Give the extent of all Plasmodium vivax-infected red blood cells.
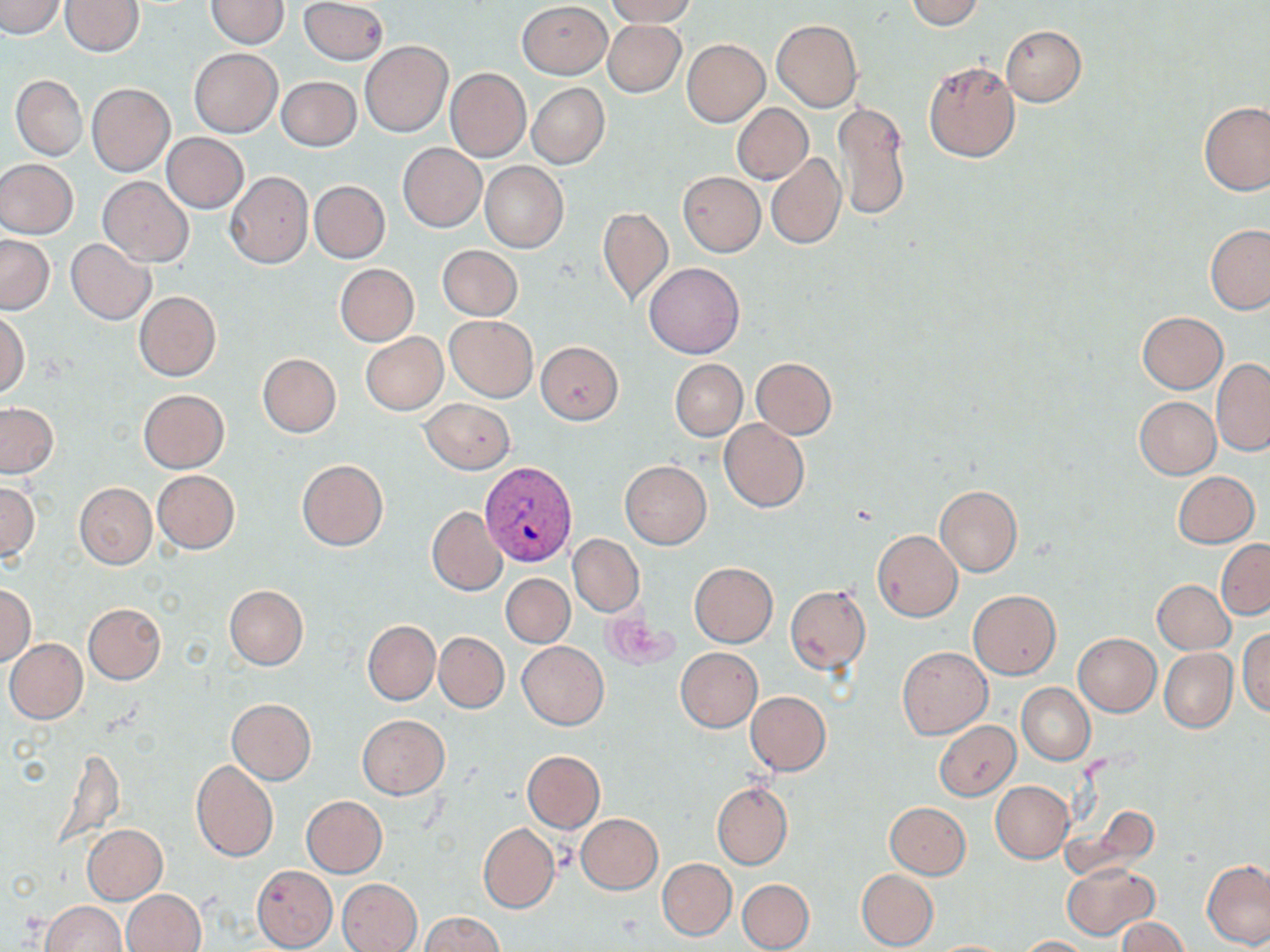
Approximate bounding boxes as named x1/y1/x2/y2 corners in pixels.
Plasmodium vivax-infected red blood cells: (x1=481, y1=461, x2=577, y2=567).

slide-level diagnosis = Plasmodium vivax
stain = May-Grünwald-Giemsa
magnification = 1000x
uninfected red blood cell locations = approximate bounding boxes as named x1/y1/x2/y2 corners in pixels: (x1=0, y1=0, x2=66, y2=38), (x1=62, y1=0, x2=143, y2=56), (x1=205, y1=0, x2=288, y2=48), (x1=604, y1=0, x2=697, y2=26), (x1=904, y1=0, x2=984, y2=29), (x1=299, y1=1, x2=388, y2=65), (x1=518, y1=1, x2=612, y2=78), (x1=771, y1=19, x2=863, y2=113), (x1=602, y1=20, x2=685, y2=96), (x1=1000, y1=25, x2=1087, y2=106), (x1=682, y1=39, x2=770, y2=127), (x1=360, y1=41, x2=452, y2=137), (x1=189, y1=49, x2=281, y2=136), (x1=924, y1=60, x2=1021, y2=163), (x1=446, y1=68, x2=531, y2=161), (x1=12, y1=75, x2=87, y2=160), (x1=277, y1=76, x2=360, y2=151), (x1=86, y1=83, x2=175, y2=177), (x1=527, y1=83, x2=609, y2=169), (x1=1198, y1=101, x2=1270, y2=195), (x1=833, y1=102, x2=910, y2=220), (x1=732, y1=103, x2=813, y2=183), (x1=162, y1=133, x2=249, y2=213), (x1=397, y1=142, x2=486, y2=232), (x1=765, y1=152, x2=846, y2=250), (x1=0, y1=158, x2=78, y2=238), (x1=480, y1=161, x2=568, y2=253), (x1=225, y1=171, x2=313, y2=268), (x1=678, y1=171, x2=764, y2=256), (x1=98, y1=178, x2=193, y2=266), (x1=309, y1=180, x2=390, y2=263), (x1=598, y1=206, x2=673, y2=309), (x1=1205, y1=224, x2=1270, y2=314), (x1=0, y1=235, x2=54, y2=315), (x1=66, y1=240, x2=155, y2=324), (x1=438, y1=245, x2=522, y2=320), (x1=644, y1=263, x2=744, y2=359), (x1=335, y1=264, x2=418, y2=345), (x1=134, y1=291, x2=221, y2=381), (x1=0, y1=311, x2=28, y2=397), (x1=1137, y1=311, x2=1229, y2=393), (x1=445, y1=316, x2=538, y2=402), (x1=360, y1=332, x2=448, y2=415), (x1=536, y1=341, x2=624, y2=424), (x1=257, y1=353, x2=342, y2=437), (x1=751, y1=357, x2=836, y2=439), (x1=670, y1=359, x2=747, y2=441), (x1=1211, y1=359, x2=1270, y2=455), (x1=138, y1=389, x2=230, y2=472), (x1=1134, y1=397, x2=1221, y2=479), (x1=420, y1=398, x2=516, y2=474), (x1=1, y1=403, x2=58, y2=477), (x1=719, y1=419, x2=810, y2=512), (x1=296, y1=459, x2=388, y2=551), (x1=620, y1=460, x2=712, y2=548), (x1=152, y1=470, x2=240, y2=554), (x1=1172, y1=471, x2=1259, y2=547), (x1=0, y1=478, x2=38, y2=564), (x1=74, y1=483, x2=156, y2=569), (x1=934, y1=485, x2=1022, y2=576), (x1=426, y1=506, x2=508, y2=596), (x1=872, y1=530, x2=963, y2=621), (x1=568, y1=534, x2=643, y2=617), (x1=1217, y1=538, x2=1270, y2=619), (x1=689, y1=562, x2=778, y2=647), (x1=501, y1=573, x2=574, y2=647), (x1=1153, y1=579, x2=1234, y2=654), (x1=1, y1=583, x2=35, y2=666), (x1=224, y1=585, x2=307, y2=670), (x1=785, y1=585, x2=870, y2=675), (x1=967, y1=590, x2=1061, y2=678), (x1=83, y1=603, x2=165, y2=685), (x1=362, y1=621, x2=440, y2=705), (x1=1237, y1=628, x2=1270, y2=717), (x1=435, y1=632, x2=509, y2=713), (x1=1073, y1=632, x2=1161, y2=716), (x1=4, y1=638, x2=88, y2=724), (x1=518, y1=642, x2=609, y2=730), (x1=897, y1=646, x2=992, y2=738), (x1=676, y1=647, x2=762, y2=732), (x1=1160, y1=647, x2=1237, y2=732), (x1=1017, y1=684, x2=1094, y2=764), (x1=745, y1=691, x2=831, y2=775), (x1=226, y1=698, x2=316, y2=784), (x1=358, y1=715, x2=449, y2=799), (x1=933, y1=721, x2=1021, y2=801), (x1=522, y1=750, x2=604, y2=833), (x1=191, y1=761, x2=279, y2=863), (x1=711, y1=781, x2=792, y2=870), (x1=991, y1=781, x2=1075, y2=863), (x1=301, y1=796, x2=387, y2=877), (x1=884, y1=802, x2=970, y2=879), (x1=1066, y1=804, x2=1155, y2=877), (x1=576, y1=814, x2=663, y2=894), (x1=478, y1=822, x2=559, y2=913), (x1=81, y1=824, x2=168, y2=904), (x1=1202, y1=858, x2=1270, y2=952), (x1=656, y1=859, x2=736, y2=940), (x1=1061, y1=862, x2=1158, y2=941), (x1=251, y1=865, x2=338, y2=951), (x1=856, y1=869, x2=939, y2=950), (x1=337, y1=878, x2=424, y2=952), (x1=738, y1=879, x2=814, y2=951), (x1=121, y1=889, x2=205, y2=952), (x1=41, y1=900, x2=127, y2=952), (x1=420, y1=913, x2=503, y2=952), (x1=1115, y1=917, x2=1187, y2=952), (x1=1015, y1=935, x2=1094, y2=951), (x1=927, y1=939, x2=1020, y2=951)
preparation = thin blood film
modality = light microscopy
image size = 1270×952 pixels
field of view = one of a larger specimen